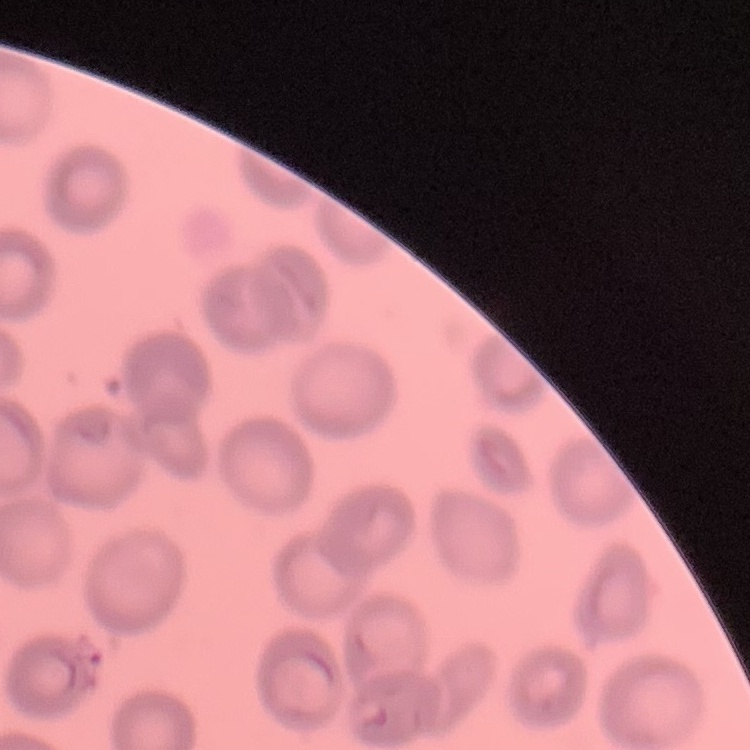
Summary:
  - Erythrocyte morphology: no rouleaux formation
  - Preparation: thin blood film
  - Stain: Field's or Giemsa
  - Image type: one tile cut from a larger photomicrograph